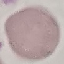
result: no malaria parasites seen
image_type: cell patch, automatically extracted from a larger field of view and resized to 64 × 64 pixels
stain: Giemsa
preparation: thin blood film
capture: smartphone camera at the microscope eyepiece